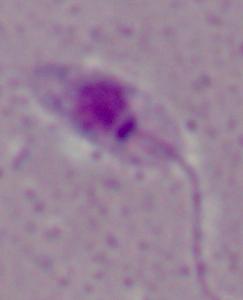 Captured at 1000x magnification. A Leishmania parasite is shown. Micrograph.